Report the malaria status of this cell.
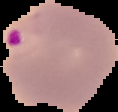
It is parasitized.

preparation = thin blood smear
image type = segmented cell region with the area outside set to black
image size = 118×112 pixels